Comment on the morphology of the erythrocytes.
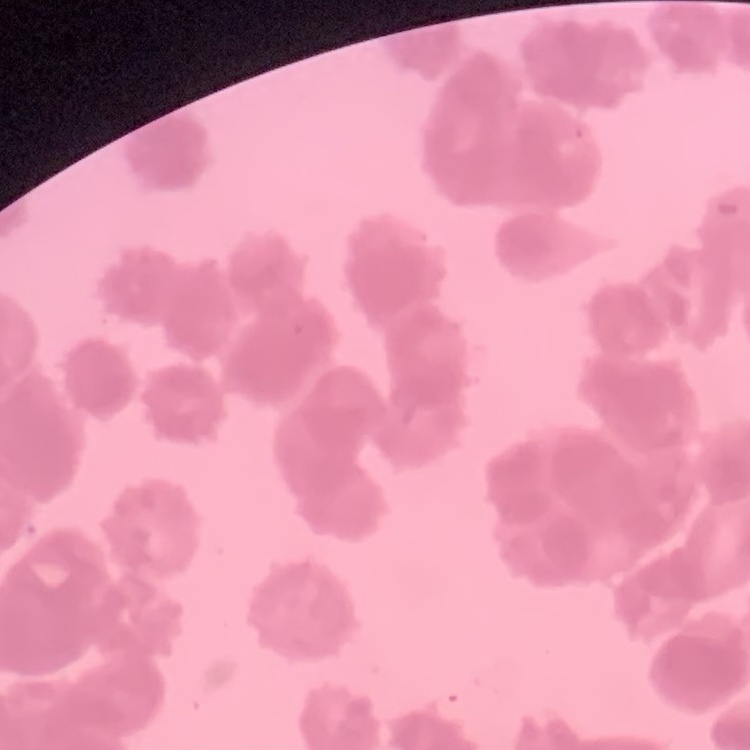
They show rouleaux formation.

Summary:
  - Preparation: thin blood film
  - Image type: one tile cut from a larger photomicrograph
  - Stain: Field's or Giemsa